Classify this cell by malaria status.
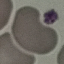
It is uninfected.

Summary:
  - Image type: cell patch, automatically extracted from a larger field of view and resized to 64 × 64 pixels
  - Preparation: thin blood film
  - Stain: Giemsa
  - Capture: smartphone camera at the microscope eyepiece